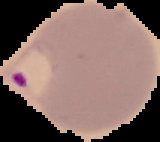

Summary:
  - Image type: segmented cell region on a black background
  - Image size: 160×142 pixels
  - Result: Plasmodium parasites identified
  - Preparation: thin blood film